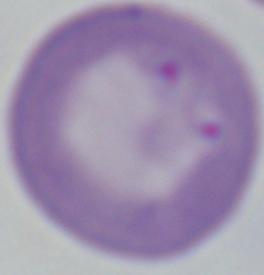
modality: photomicrograph
magnification: 1000x
identification: Babesia